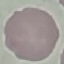
result = no malaria parasites seen
capture = smartphone camera at the microscope eyepiece
preparation = thin blood smear
stain = Giemsa
image type = automatically extracted cell patch, resized to 64 × 64 pixels